Report the malaria status of this cell.
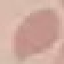

It is uninfected.

Thin blood smear. Cell patch, automatically extracted from a larger field of view and resized to 64 × 64 pixels. Acquired by smartphone through the microscope eyepiece. Giemsa stain.